Classify this cell by malaria status.
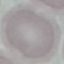

Uninfected.

Thin smear of blood. Cell patch, automatically extracted from a larger field of view and resized to 64 × 64 pixels. Acquired by smartphone through the microscope eyepiece. Giemsa-stained preparation.